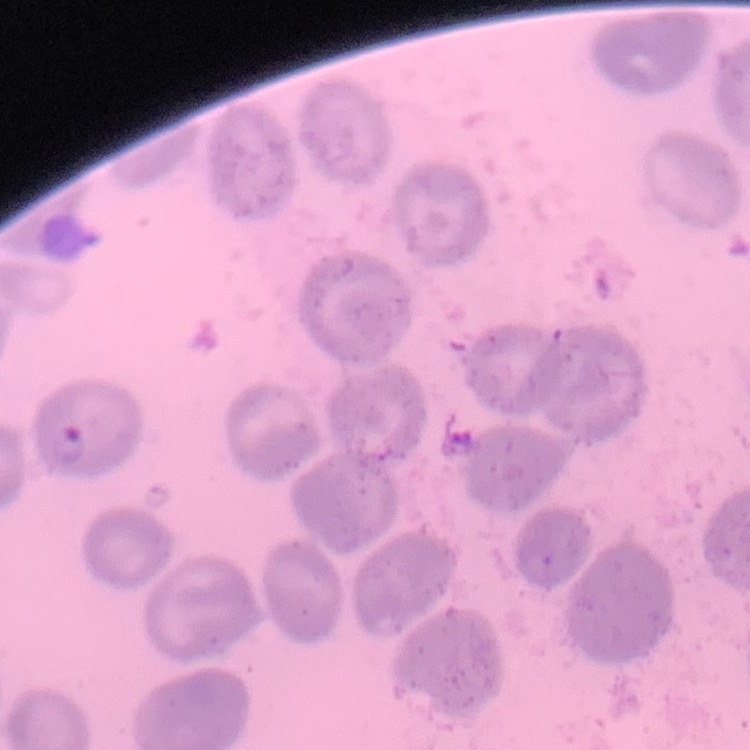

Summary:
  - Erythrocyte morphology: no rouleaux formation
  - Image type: one tile cut from a larger photomicrograph
  - Stain: Field's or Giemsa
  - Preparation: thin blood smear